State the blood parasite species.
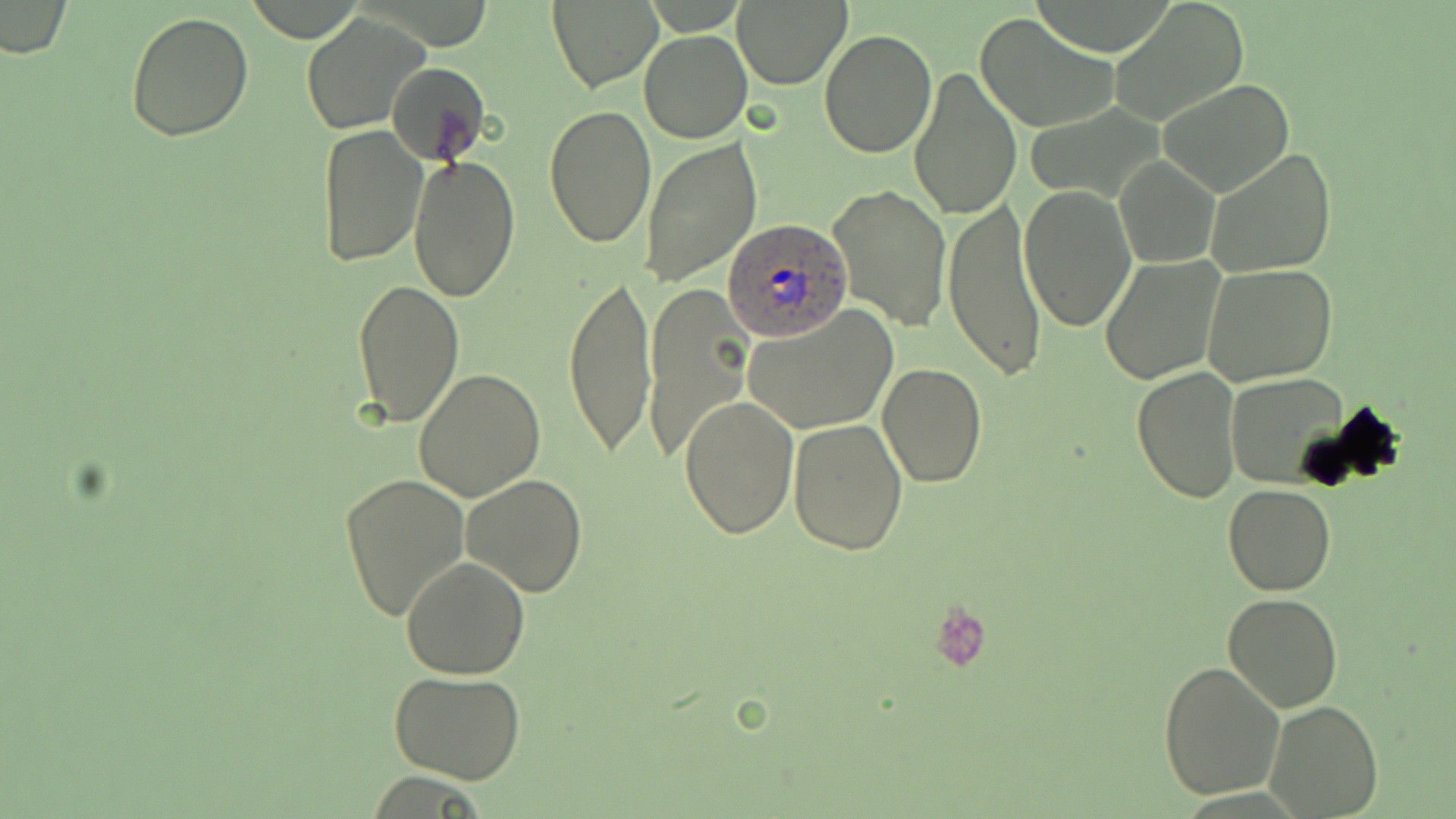
Plasmodium ovale.

Approximate bounding boxes as [x1, y1, x2, y2] in pixels. Uninfected red blood cell locations: [547, 1, 661, 91], [732, 2, 850, 88], [2, 3, 73, 58], [1111, 3, 1248, 126], [124, 9, 255, 142], [301, 11, 430, 135], [973, 12, 1117, 133], [819, 27, 937, 157], [640, 30, 752, 143], [386, 61, 491, 169], [908, 66, 1023, 221], [1156, 79, 1297, 199], [544, 103, 657, 248], [317, 124, 430, 269], [639, 140, 761, 286], [1205, 147, 1336, 279], [408, 153, 521, 303], [1114, 155, 1220, 269], [827, 183, 952, 332], [1021, 184, 1137, 332], [942, 200, 1047, 381], [1099, 256, 1226, 384], [1202, 264, 1338, 387], [563, 272, 656, 460], [353, 278, 463, 427], [644, 286, 753, 467], [743, 305, 897, 435], [878, 362, 987, 488], [1132, 365, 1244, 504], [414, 368, 547, 503], [1228, 374, 1349, 489], [677, 395, 800, 541], [788, 418, 909, 556], [339, 473, 470, 623], [461, 473, 588, 597], [1223, 485, 1335, 595], [400, 558, 531, 679], [1223, 593, 1343, 711], [1159, 659, 1286, 801], [390, 671, 527, 785], [1265, 701, 1384, 817]. Plasmodium ovale-infected red blood cell locations: [724, 216, 853, 341]. Platelet locations: [927, 599, 992, 674]. May-Grünwald-Giemsa stain. Captured at 1000x magnification. Thin blood film. Image is 1456×819 pixels. One field of a larger specimen. Optical microscopy.